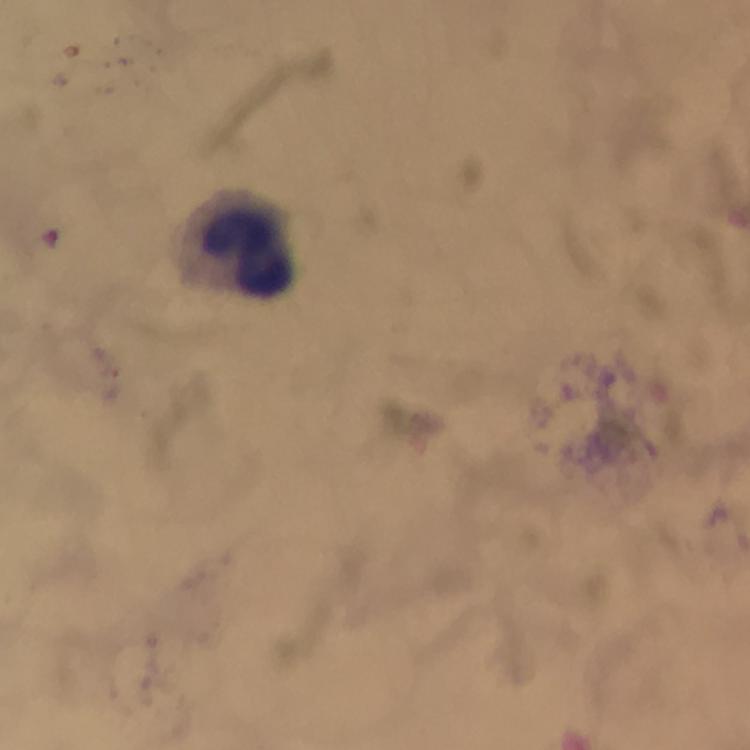
cropped from = one field of view
image size = 750×750 pixels
capture = smartphone mounted on the microscope
preparation = thick smear
magnification = 100x
immersion oil = applied
stain = Giemsa
leukocyte locations = approximate centers as (x, y) in pixels: (248, 255)
Plasmodium parasites = none detected
context = from a diagnostic examination for malaria